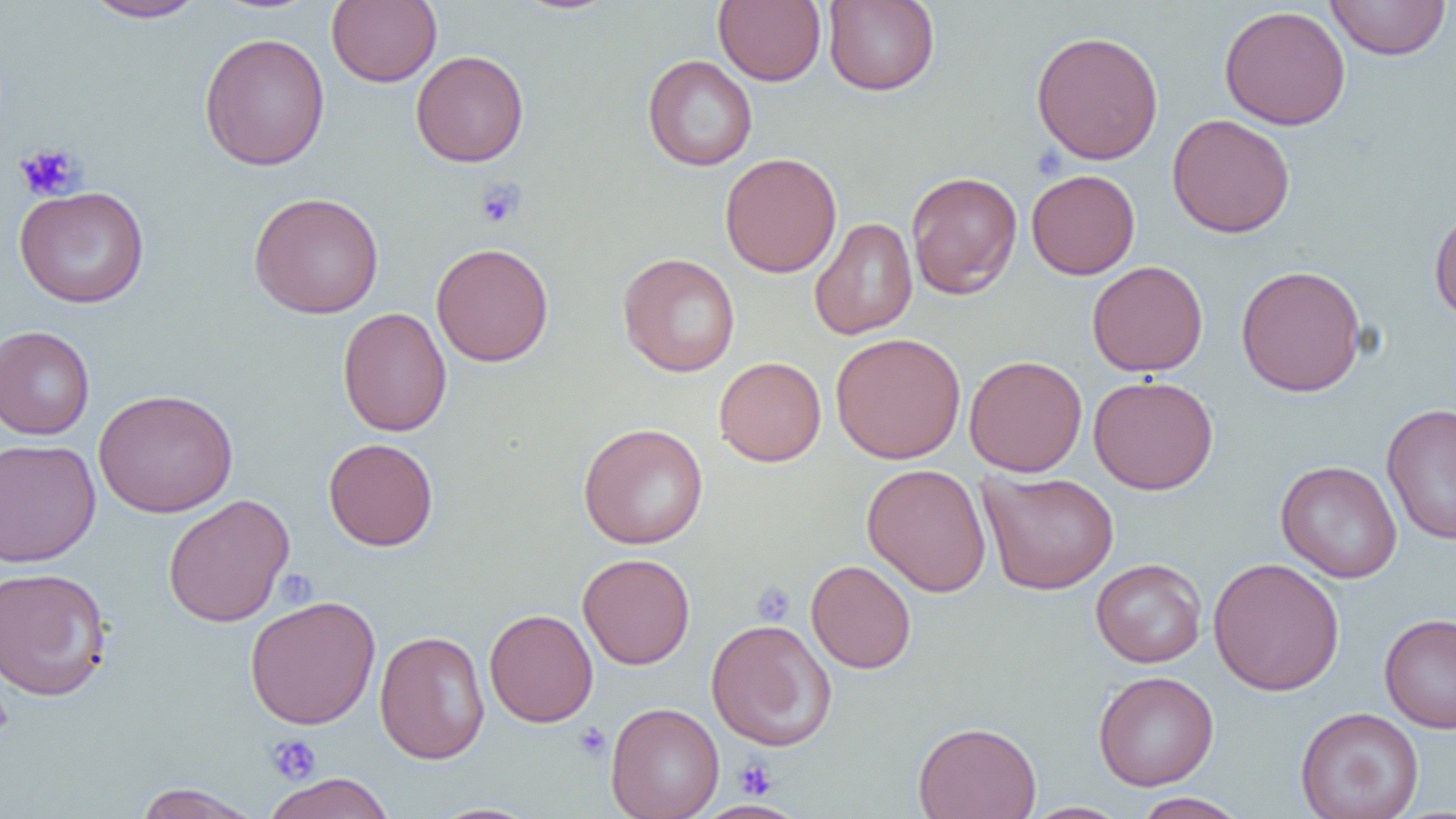

slide-level diagnosis = negative for blood parasites
image size = 1456×819 pixels
field of view = single
uninfected red blood cell locations = approximate bounding boxes as (x1,y1)-(x2,y2) corner pairs in pixels: (82,0)-(209,22), (326,0)-(442,87), (512,0)-(621,15), (713,0)-(826,86), (823,0)-(939,96), (1324,0)-(1452,60), (1219,5)-(1351,130), (1030,30)-(1164,165), (199,32)-(330,171), (411,50)-(529,167), (642,54)-(758,171), (1167,113)-(1296,238), (720,152)-(842,278), (1026,169)-(1140,279), (905,170)-(1022,299), (14,185)-(149,308), (248,192)-(385,318), (1429,204)-(1456,324), (809,216)-(918,340), (431,242)-(554,367), (618,252)-(741,377), (1087,260)-(1209,376), (1235,264)-(1367,397), (337,306)-(452,437), (0,325)-(95,440), (830,332)-(966,464), (964,355)-(1087,477), (714,356)-(826,467), (1088,375)-(1219,495), (93,388)-(238,518), (1382,403)-(1456,545), (578,422)-(709,549), (323,437)-(438,551), (0,438)-(101,568), (1276,460)-(1403,582), (862,463)-(992,597), (978,470)-(1119,595), (162,494)-(295,627), (577,552)-(695,669), (1208,557)-(1345,697), (1090,558)-(1207,667), (805,560)-(916,674), (0,566)-(113,701), (244,595)-(382,730), (484,609)-(598,727), (1379,612)-(1456,734), (705,618)-(837,751), (374,623)-(598,742), (374,630)-(491,764), (1093,670)-(1219,790), (605,702)-(725,819), (1295,707)-(1424,819), (913,721)-(1042,819), (263,772)-(396,819), (131,783)-(262,818), (1132,792)-(1249,819), (693,800)-(808,818), (424,802)-(545,819), (1021,802)-(1133,819)
modality = light microscopy
platelet locations = approximate bounding boxes as (x1,y1)-(x2,y2) corner pairs in pixels: (14,143)-(84,201), (474,179)-(526,230), (752,581)-(796,626), (573,723)-(611,761), (265,734)-(321,784), (733,757)-(777,799)
magnification = 1000x
preparation = thin blood smear